Locate and identify every blood parasite.
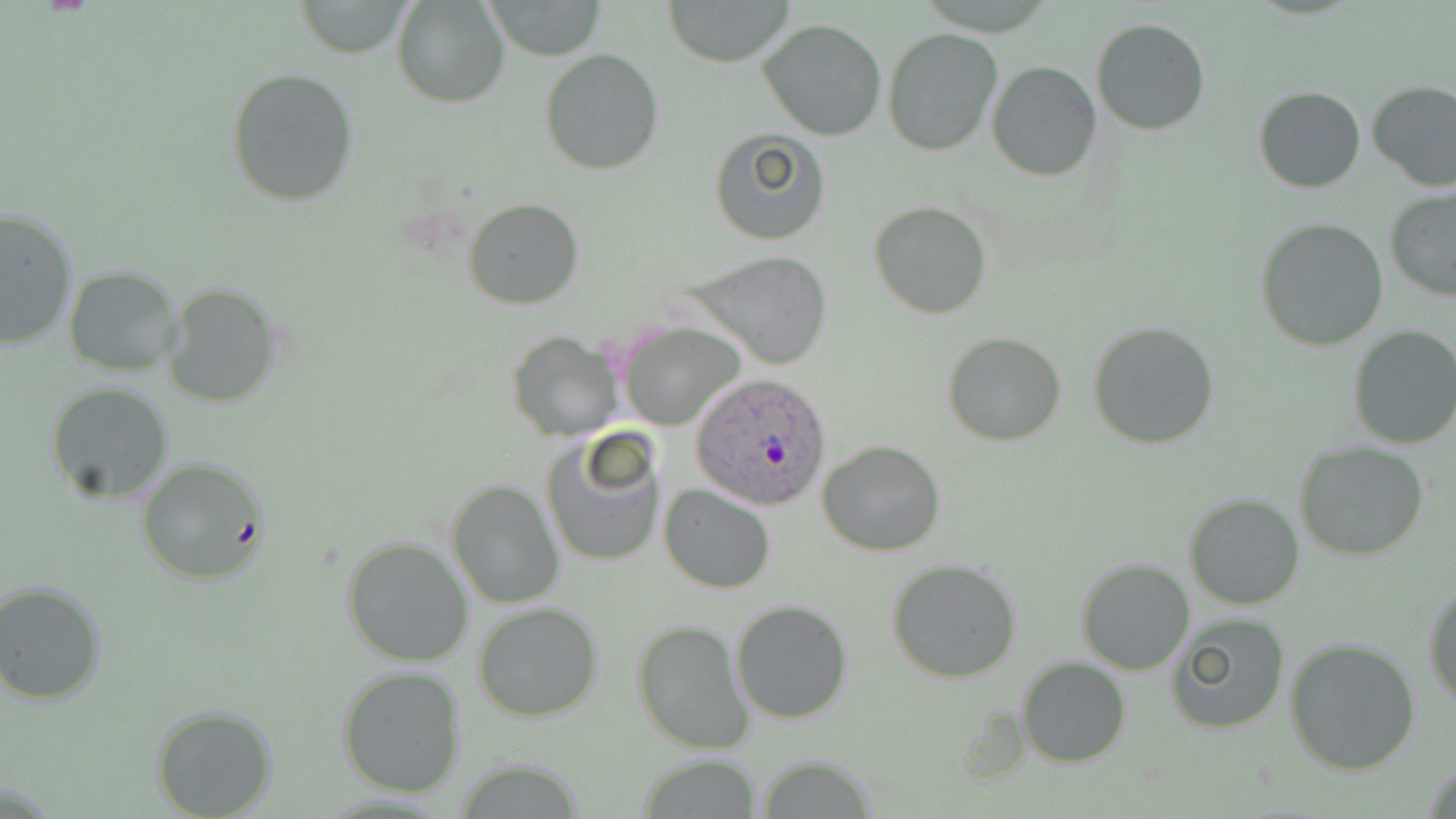

Approximate bounding boxes as (x1,y1)-(x2,y2) corner pairs in pixels.
Plasmodium ovale-infected red blood cells: (692,372)-(833,512).
No Plasmodium falciparum, Plasmodium malariae, Plasmodium vivax, Babesia divergens, or Trypanosoma brucei observed.

Summary:
  - Uninfected red blood cell locations: (393,0)-(509,107), (485,0)-(606,60), (663,0)-(794,66), (293,1)-(416,57), (757,18)-(888,141), (1090,18)-(1213,137), (883,29)-(1001,156), (540,48)-(666,176), (986,62)-(1101,182), (226,68)-(361,207), (1367,79)-(1456,192), (1253,86)-(1365,193), (708,129)-(830,246), (1384,189)-(1456,302), (464,197)-(583,309), (869,201)-(994,319), (1,206)-(77,351), (1256,219)-(1389,352), (691,251)-(834,371), (64,265)-(184,378), (161,282)-(284,411), (620,320)-(745,431), (1087,320)-(1218,449), (1347,325)-(1456,450), (507,329)-(625,442), (943,333)-(1065,445), (45,382)-(174,504), (541,430)-(665,569), (818,440)-(946,555), (1295,441)-(1430,561), (136,458)-(268,584), (446,479)-(564,609), (660,485)-(776,594), (1185,493)-(1305,609), (341,535)-(476,669), (1075,558)-(1194,675), (888,559)-(1022,682), (1423,573)-(1456,710), (0,579)-(106,706), (731,599)-(853,723), (472,603)-(603,721), (1166,614)-(1291,734), (631,618)-(755,755), (1285,637)-(1422,775), (1017,658)-(1132,768), (336,666)-(467,799), (151,704)-(277,818), (634,757)-(768,817)
  - Slide-level diagnosis: Plasmodium ovale
  - Preparation: thin blood smear
  - Magnification: 1000x
  - Modality: optical microscopy
  - Stain: May-Grünwald-Giemsa
  - Image size: 1456×819 pixels
  - Field of view: single